Assess for parasitized red blood cells.
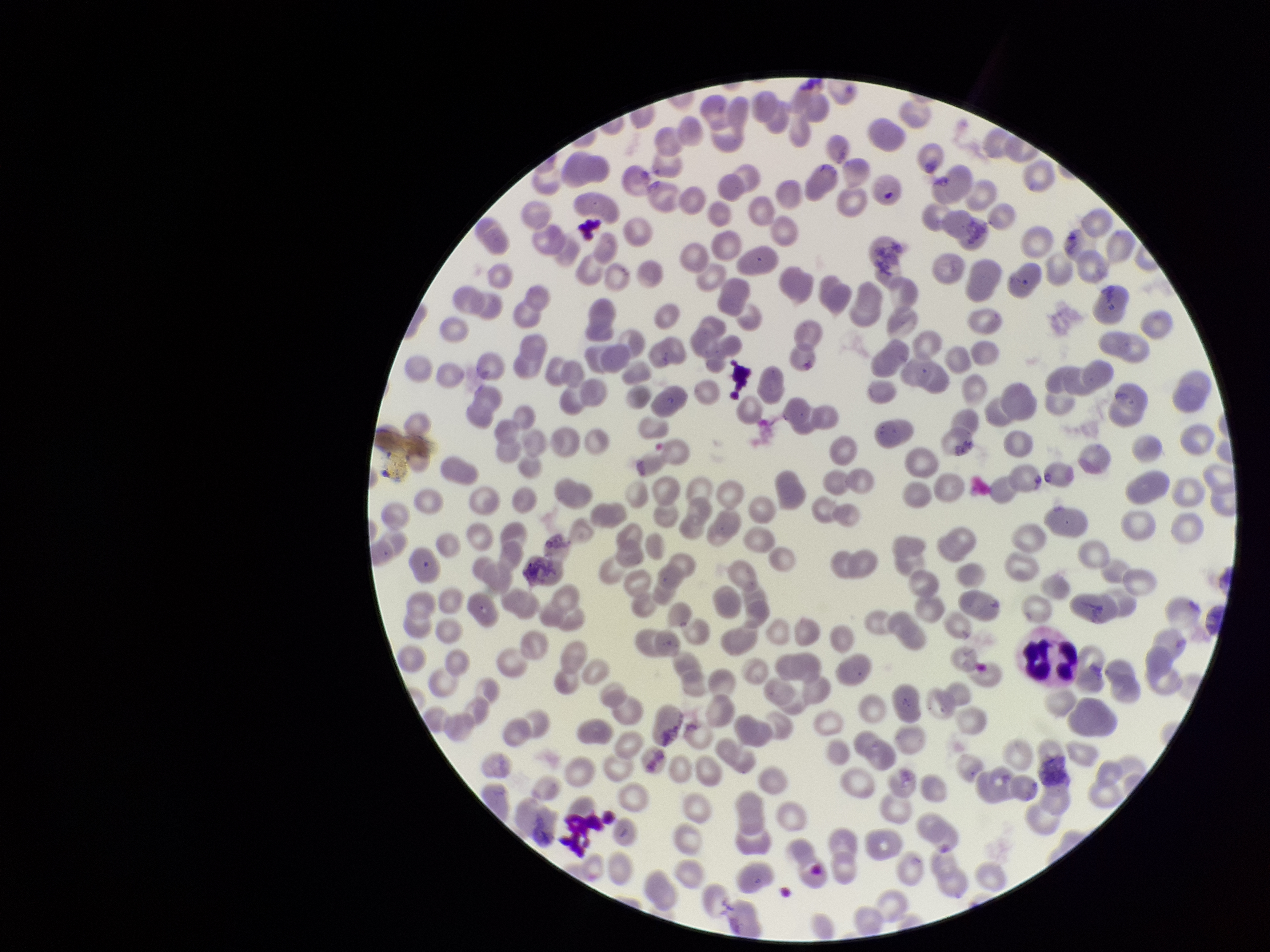

None detected.

Summary:
  - Patient malaria status: negative
  - Preparation: thin smear
  - Red blood cell count: 260
  - Field of view: one from this slide
  - Parasitized red blood cell count: 0
  - Stain: Giemsa
  - Image size: 1270×952 pixels
  - Capture: smartphone photograph through the microscope eyepiece